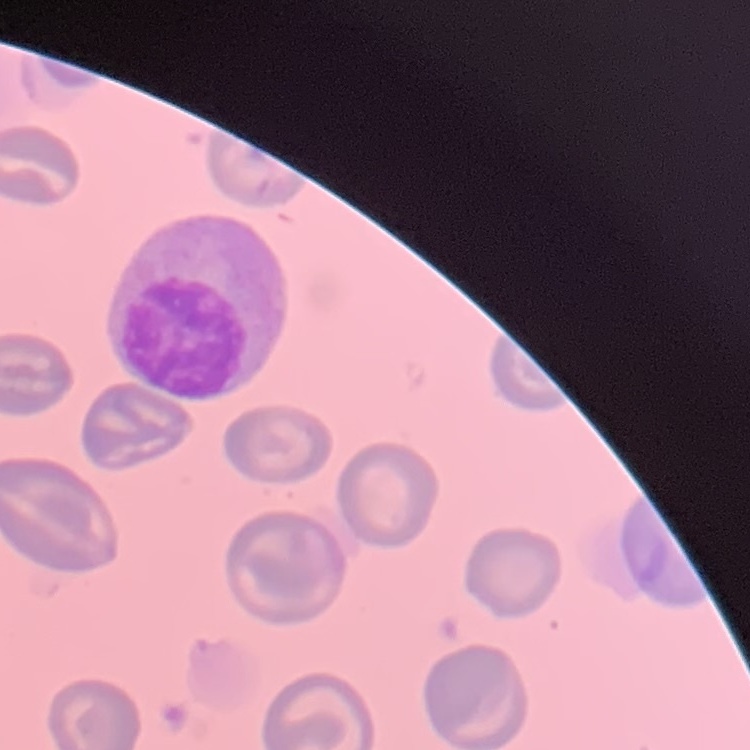
The erythrocytes show no rouleaux formation. Stained with either Field's or Giemsa. One tile cut from a larger photomicrograph. Thin blood smear.